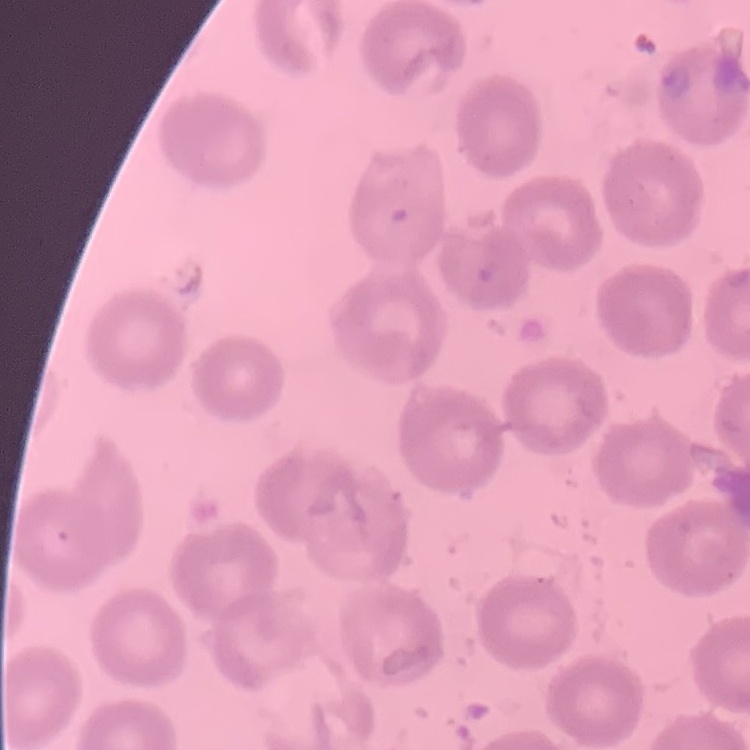
{
  "red_blood_cell_morphology": "no rouleaux formation",
  "stain": "Field's or Giemsa",
  "preparation": "thin peripheral smear",
  "image_type": "square crop of a larger photomicrograph"
}